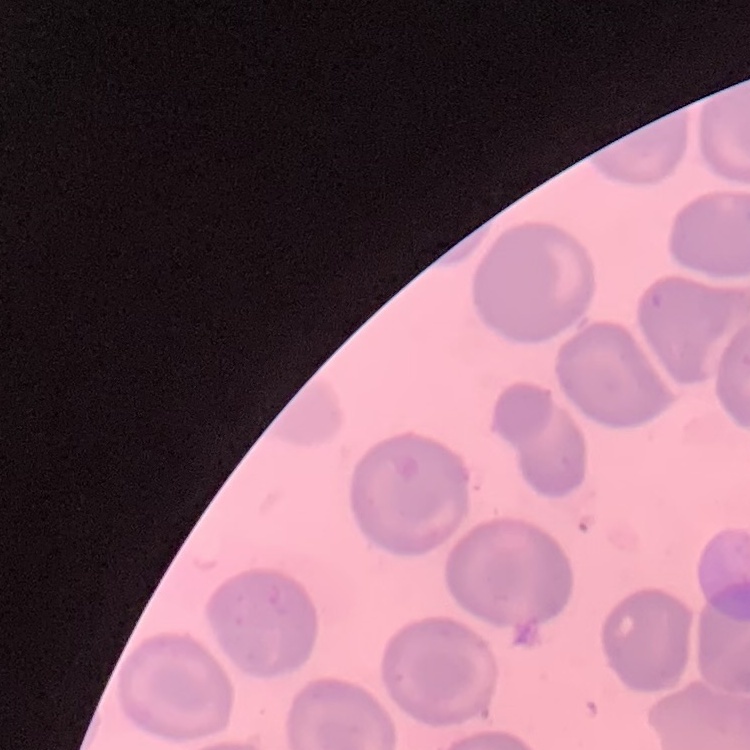

Summary:
  - Red blood cell morphology: no rouleaux formation
  - Stain: Field's or Giemsa
  - Preparation: thin peripheral smear
  - Image type: one tile cut from a larger photomicrograph